Point out every Plasmodium parasite.
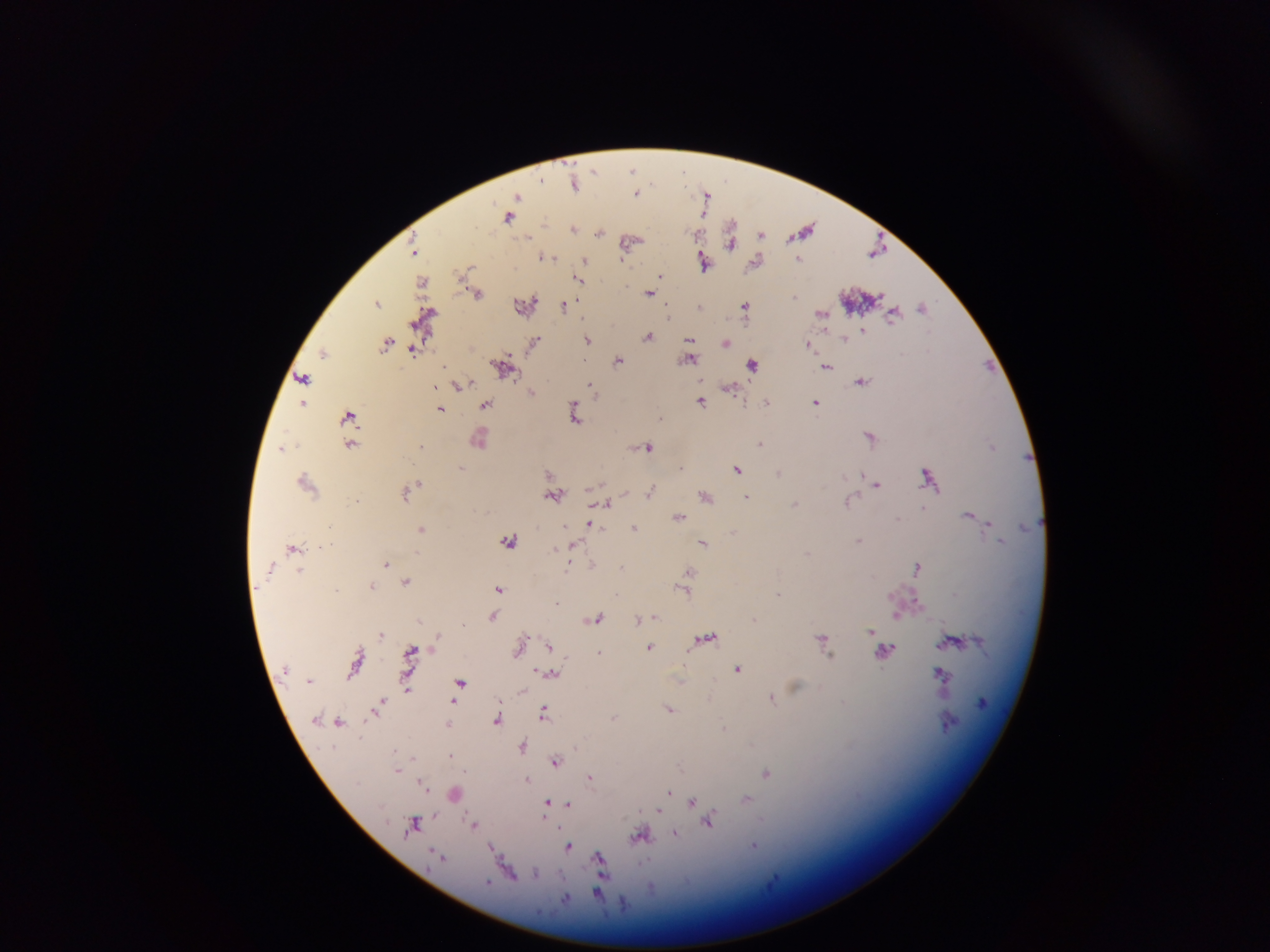
Approximate centers as {x, y} in pixels.
Plasmodium parasites: {633, 171}, {575, 183}, {638, 193}, {707, 194}, {518, 196}, {509, 217}, {574, 227}, {804, 230}, {600, 231}, {697, 233}, {762, 234}, {731, 239}, {630, 242}, {415, 249}, {877, 251}, {543, 255}, {585, 259}, {799, 259}, {705, 261}, {757, 261}, {467, 269}, {661, 275}, {581, 279}, {422, 281}, {650, 292}, {477, 293}, {860, 298}, {378, 302}, {525, 303}, {565, 304}, {701, 305}, {746, 306}, {923, 307}, {895, 312}, {822, 314}, {425, 318}, {863, 330}, {649, 336}, {844, 337}, {691, 339}, {589, 340}, {534, 342}, {388, 343}, {726, 343}, {809, 344}, {414, 350}, {324, 352}, {690, 356}, {620, 359}, {753, 364}, {505, 365}, {989, 365}, {826, 366}, {303, 377}, {862, 381}, {460, 384}, {435, 386}, {593, 386}, {730, 387}, {533, 391}, {767, 400}, {702, 401}, {816, 401}, {303, 403}, {487, 404}, {441, 409}, {575, 411}, {349, 415}, {661, 416}, {871, 436}, {480, 437}, {761, 442}, {350, 445}, {282, 446}, {422, 446}, {648, 446}, {463, 467}, {738, 469}, {779, 472}, {930, 475}, {306, 481}, {419, 482}, {877, 484}, {414, 487}, {406, 491}, {651, 491}, {707, 494}, {554, 495}, {747, 497}, {850, 500}, {609, 502}, {796, 503}, {925, 506}, {970, 513}, {680, 515}, {590, 522}, {989, 522}, {422, 528}, {635, 528}, {510, 540}, {860, 540}, {1002, 540}, {705, 542}, {574, 543}, {294, 548}, {387, 563}, {592, 564}, {918, 566}, {690, 572}, {407, 581}, {689, 584}, {373, 585}, {499, 588}, {687, 590}, {779, 593}, {558, 601}, {897, 614}, {655, 615}, {493, 616}, {598, 618}, {639, 620}, {872, 631}, {382, 634}, {706, 637}, {824, 640}, {953, 641}, {521, 642}, {550, 645}, {650, 646}, {887, 649}, {412, 650}, {600, 653}, {356, 666}, {739, 668}, {553, 673}, {941, 673}, {408, 681}, {461, 682}, {406, 688}, {772, 697}, {453, 702}, {380, 704}, {376, 708}, {670, 708}, {545, 711}, {498, 718}, {614, 718}, {338, 721}, {449, 724}, {725, 727}, {523, 745}, {576, 747}, {450, 755}, {413, 757}, {556, 760}, {398, 770}, {466, 771}, {767, 772}, {591, 776}, {528, 779}, {422, 784}, {670, 792}, {455, 793}, {748, 798}, {548, 802}, {693, 803}, {568, 805}, {660, 810}, {710, 820}, {415, 821}, {474, 824}, {676, 832}, {642, 836}, {755, 845}, {569, 847}, {491, 848}, {601, 858}, {536, 872}, {600, 893}.

field of view = single
capture = mobile-phone photograph through a microscope
country = Ghana
preparation = thick blood smear
image size = 1270×952 pixels